Report the malaria status of this cell.
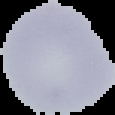
It is uninfected.

preparation = thin blood film
image type = segmented cell region with the area outside set to black
image size = 115×115 pixels